Classify this cell by malaria status.
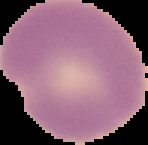

Parasitized.

image size = 148×145 pixels
preparation = thin blood film
image type = segmented cell region with the area outside set to black